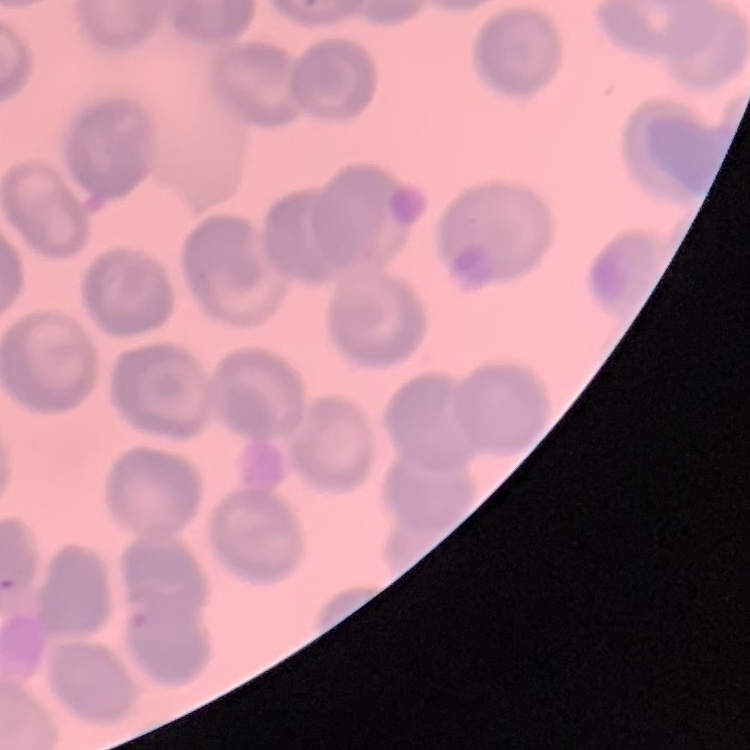

red blood cell morphology = no rouleaux formation
image type = one tile cut from a larger photomicrograph
preparation = thin blood smear
stain = Field's or Giemsa